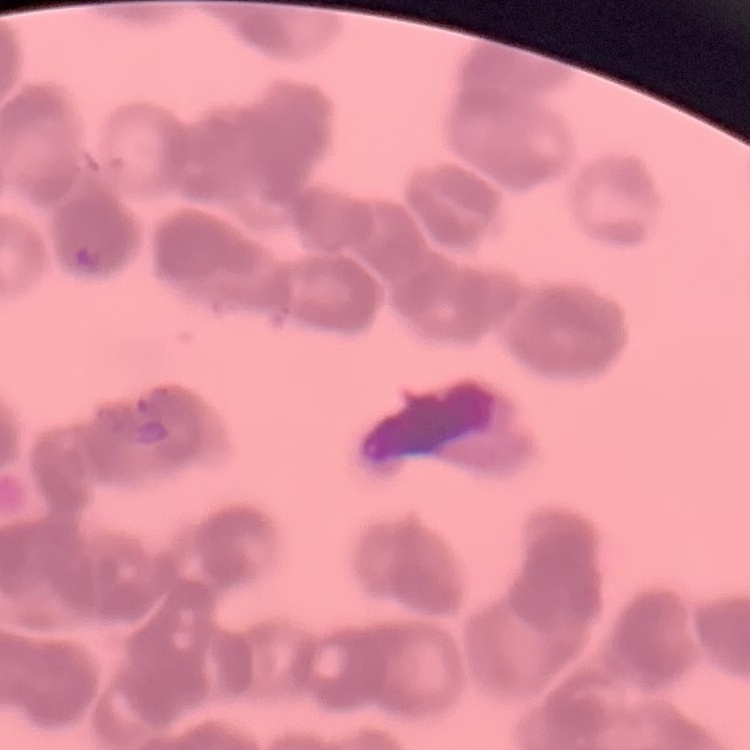
{
  "red_blood_cell_morphology": "rouleaux formation",
  "stain": "Field's or Giemsa",
  "preparation": "thin blood smear",
  "image_type": "square crop of a larger photomicrograph"
}